State which parasite is depicted.
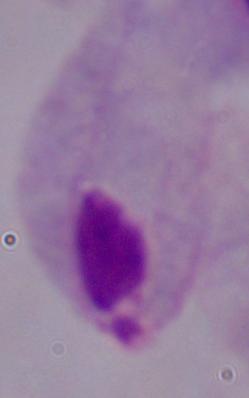

This is a trichomonad.

{
  "modality": "micrograph",
  "magnification": "1000x"
}